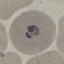

result = malaria parasites identified
image type = cell patch, automatically extracted from a larger field of view and resized to 64 × 64 pixels
preparation = thin smear
capture = smartphone camera at the microscope eyepiece
stain = Giemsa